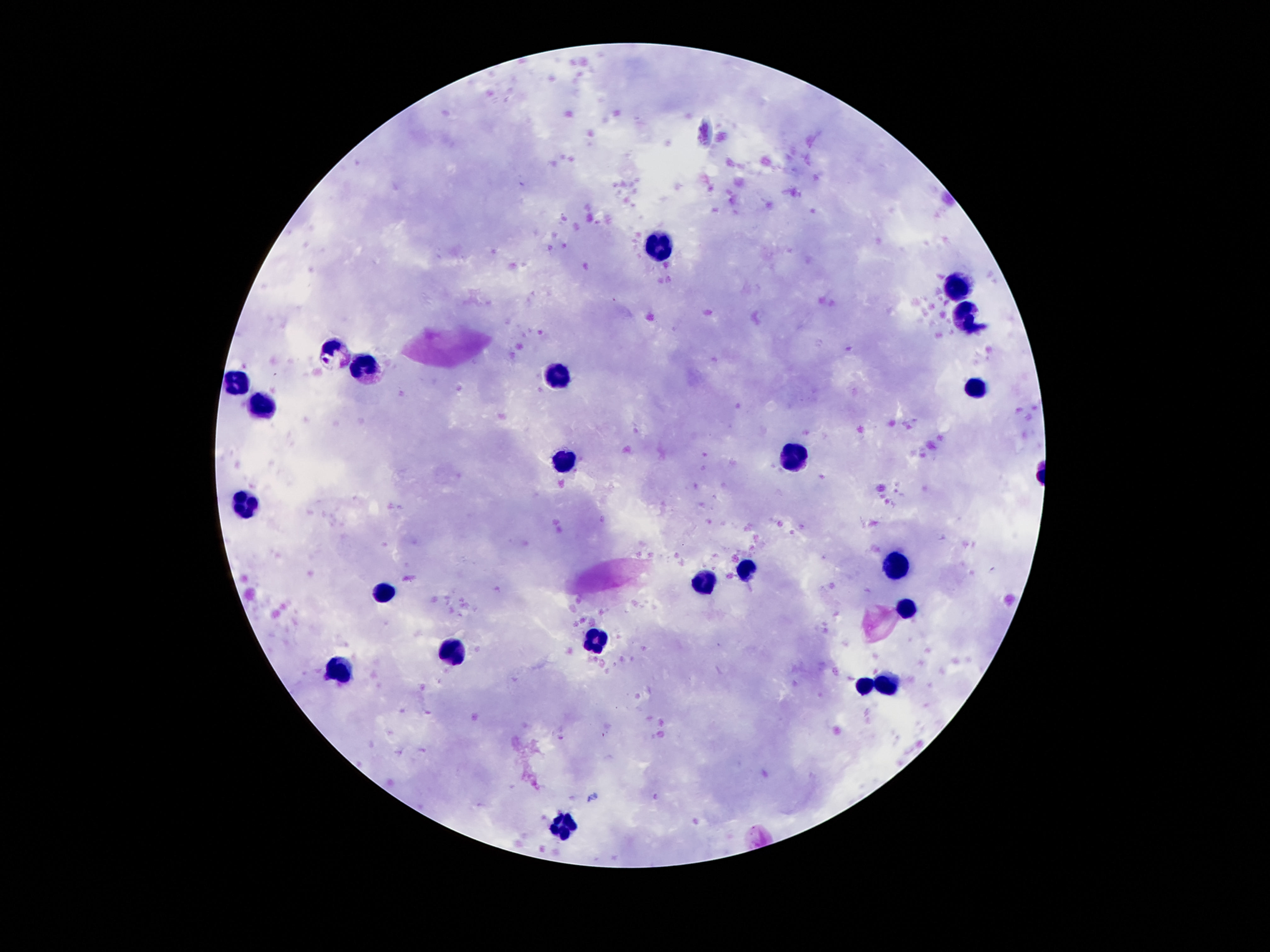
Approximate object centers, in pixels from the top-left corner. Leukocyte locations: (x=657, y=247), (x=960, y=286), (x=964, y=318), (x=335, y=351), (x=367, y=368), (x=557, y=374), (x=237, y=382), (x=972, y=390), (x=263, y=407), (x=792, y=461), (x=564, y=463), (x=244, y=507), (x=894, y=568), (x=745, y=570), (x=706, y=580), (x=386, y=593), (x=908, y=610), (x=594, y=640), (x=454, y=654), (x=340, y=670), (x=864, y=686), (x=887, y=686), (x=566, y=826). Smartphone photograph taken through the microscope eyepiece. One field from this slide. 100x magnification. Image is 1270×952 pixels. Thick peripheral-blood smear. Patient malaria status: uninfected. Giemsa-stained preparation.